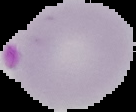
Summary:
  - Image size: 136×112 pixels
  - Malaria status: parasitized
  - Preparation: thin blood smear
  - Image type: segmented cell region with the area outside set to black